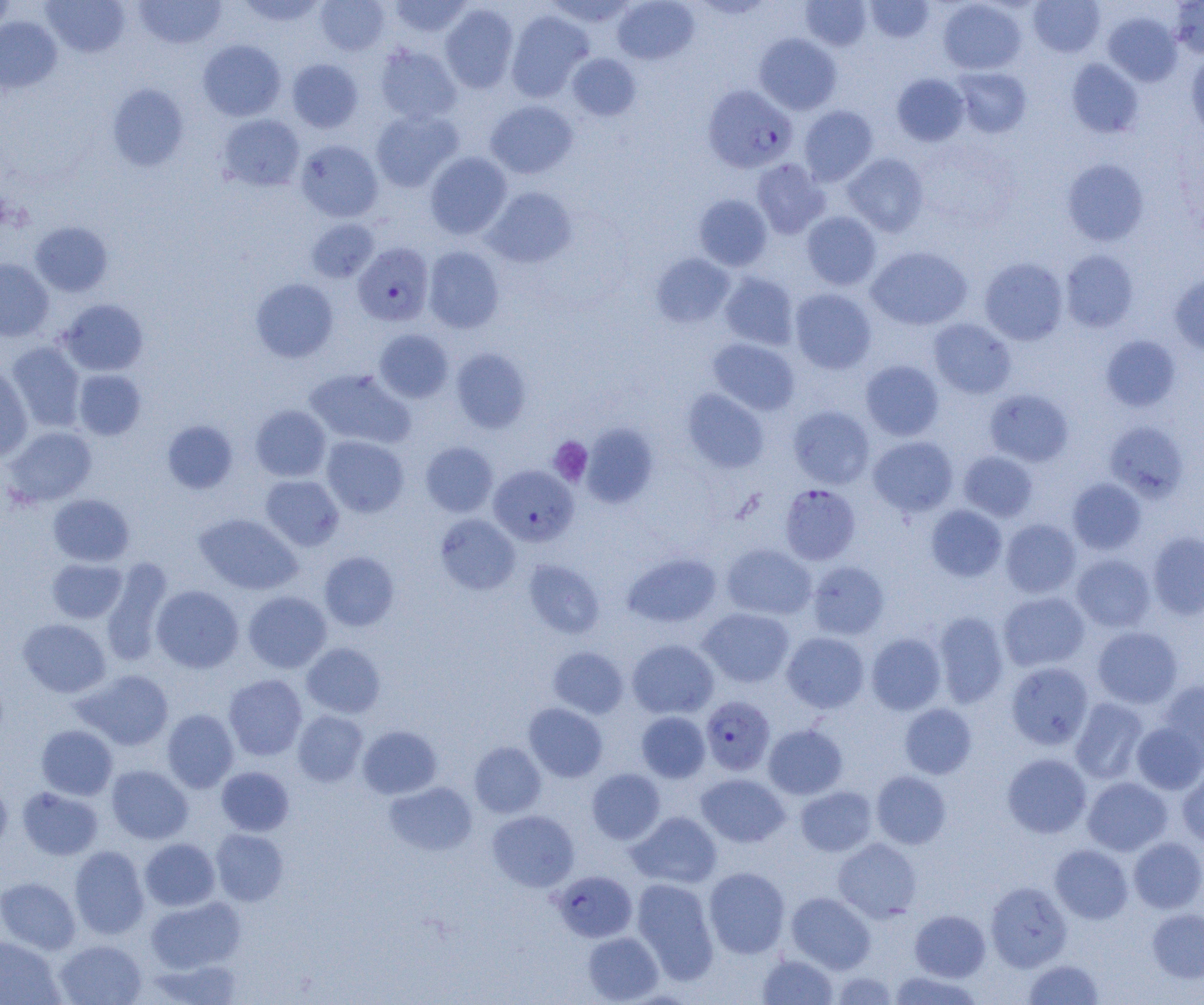
Approximate bounding boxes as (x1,y1)-(x2,y2) corner pairs in pixels. Plasmodium falciparum-infected red blood cell locations: (702,84)-(797,173), (353,243)-(434,325), (488,464)-(578,546), (784,485)-(866,566), (701,696)-(775,776), (552,870)-(637,943). Uninfected red blood cell locations: (0,0)-(15,35), (42,0)-(130,58), (134,0)-(227,49), (236,0)-(327,28), (389,0)-(472,37), (544,0)-(637,28), (612,0)-(700,65), (865,0)-(934,42), (1029,0)-(1104,57), (316,1)-(389,56), (801,1)-(872,51), (938,1)-(1026,75), (1170,1)-(1204,59), (440,3)-(518,93), (506,10)-(593,102), (1102,11)-(1182,86), (0,16)-(62,93), (754,33)-(842,115), (198,39)-(286,121), (375,45)-(461,124), (1186,52)-(1204,139), (567,53)-(641,121), (286,59)-(363,133), (1066,59)-(1144,138), (952,67)-(1031,138), (892,73)-(969,146), (107,84)-(189,171), (485,99)-(578,179), (799,105)-(878,185), (371,109)-(463,191), (218,114)-(305,191), (295,139)-(383,222), (424,151)-(512,239), (842,153)-(929,236), (751,158)-(830,239), (1062,158)-(1149,246), (483,187)-(577,268), (693,194)-(772,271), (801,211)-(881,290), (306,219)-(379,283), (30,222)-(112,296), (866,246)-(972,330), (423,247)-(504,333), (1060,250)-(1139,332), (651,253)-(735,327), (980,257)-(1068,345), (0,259)-(54,341), (719,272)-(799,350), (1169,272)-(1204,356), (251,278)-(338,362), (789,288)-(877,374), (58,299)-(149,376), (928,318)-(1016,398), (374,329)-(454,402), (1100,335)-(1181,412), (708,338)-(800,415), (5,342)-(86,432), (451,348)-(532,433), (860,360)-(944,441), (0,365)-(33,461), (305,368)-(415,450), (74,369)-(146,440), (681,388)-(769,473), (984,389)-(1074,466), (250,405)-(331,481), (788,405)-(875,488), (162,420)-(239,495), (1105,421)-(1189,501), (581,423)-(658,508), (4,426)-(97,507), (321,435)-(409,517), (868,436)-(958,516), (420,441)-(498,517), (958,450)-(1038,521), (260,475)-(344,550), (1067,478)-(1146,554), (48,494)-(134,566), (926,505)-(1007,582), (194,513)-(302,595), (435,514)-(520,595), (1000,519)-(1081,598), (1147,531)-(1204,620), (721,544)-(816,620), (319,551)-(399,631), (622,552)-(721,628), (1071,554)-(1155,632), (47,558)-(126,623), (101,559)-(173,666), (523,560)-(605,638), (807,560)-(890,639), (152,585)-(243,673), (243,591)-(332,673), (998,591)-(1090,672), (699,607)-(794,687), (933,611)-(1009,708), (18,618)-(111,698), (1092,626)-(1183,708), (782,632)-(870,713), (866,633)-(946,715), (627,639)-(719,718), (302,643)-(385,718), (548,647)-(629,718), (1006,662)-(1093,749), (76,669)-(174,750), (224,674)-(307,760), (1158,679)-(1204,758), (1070,698)-(1149,784), (523,702)-(607,782), (899,703)-(977,778), (162,709)-(239,792), (292,710)-(368,787), (636,711)-(710,782), (1131,721)-(1204,794), (763,724)-(847,799), (36,725)-(118,800), (357,725)-(442,799), (469,741)-(546,817), (1002,753)-(1091,838), (106,765)-(193,844), (217,766)-(294,836), (1177,767)-(1204,848), (587,768)-(665,844), (871,770)-(952,849), (696,773)-(790,847), (1082,777)-(1172,855), (0,778)-(12,856), (384,781)-(477,856), (795,786)-(877,856), (17,787)-(103,860), (487,810)-(579,892), (627,811)-(722,888), (211,829)-(289,906), (1129,836)-(1204,913), (139,838)-(220,911), (833,838)-(922,922), (1050,844)-(1133,924), (69,845)-(150,939), (704,867)-(790,958), (0,876)-(80,954), (632,878)-(719,983), (986,881)-(1072,971), (786,892)-(876,973), (146,896)-(245,973), (1146,908)-(1204,983), (910,910)-(990,981), (582,931)-(663,1004), (0,936)-(63,1005), (54,939)-(147,1004), (756,954)-(839,1005), (147,957)-(244,1005), (1023,959)-(1104,1004), (888,971)-(984,1004), (831,972)-(898,1004). Platelet locations: (549,436)-(593,486). Slide-level diagnosis: Plasmodium falciparum. 1000x magnification. Thin blood film. Light microscopy. One field of a larger specimen. Image is 1204×1005 pixels.